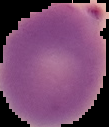 Segmented cell region on a black background. From a thin blood smear. Image is 109×127 pixels. Result: malaria parasites identified.